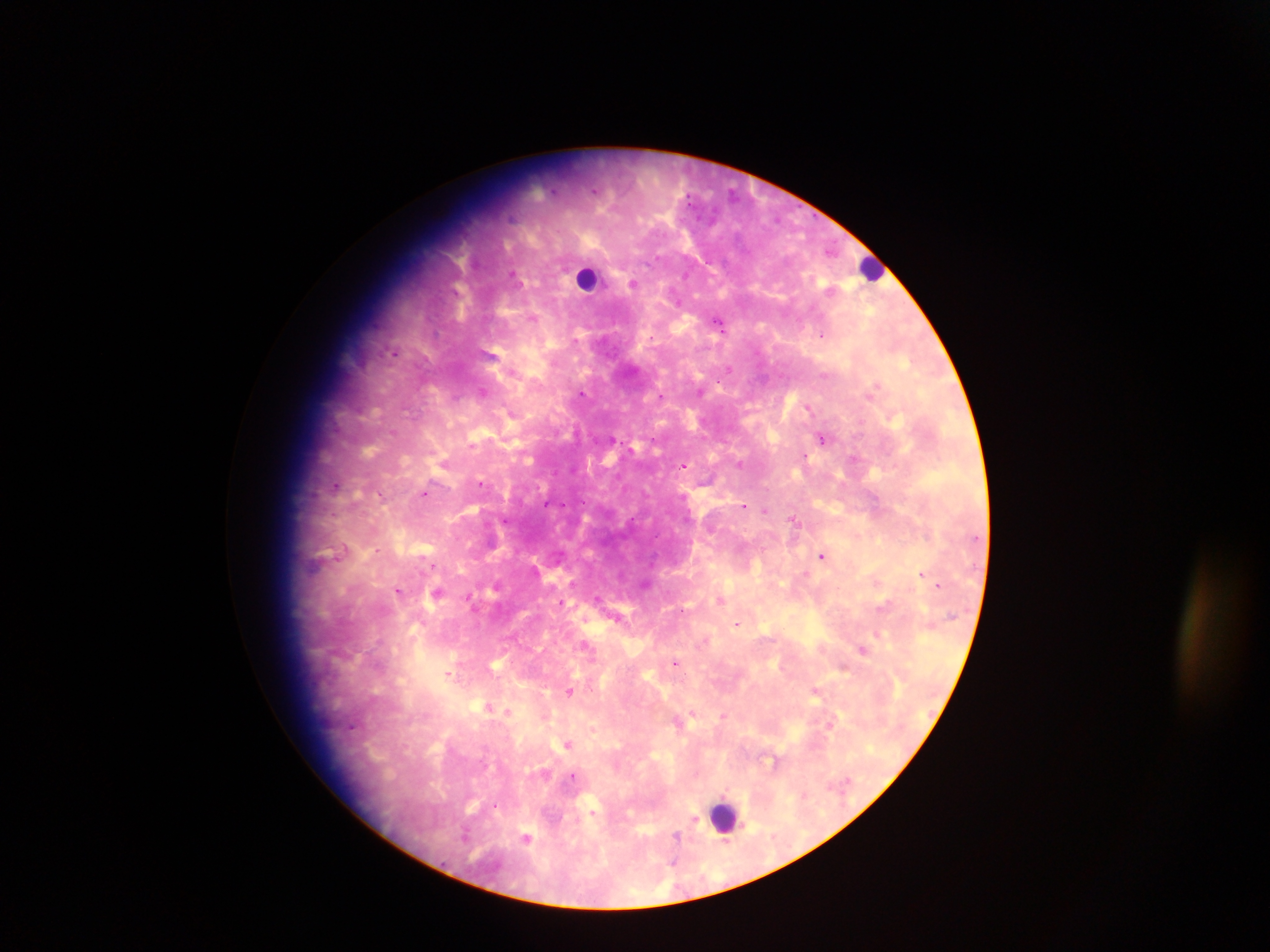
malaria_parasite_locations: 'approximate centers as x y in pixels: 633 283; 533 318; 720 321; 823 334; 394 352; 484 391; 582 393; 661 396; 808 407; 512 414; 822 437; 854 459; 445 463; 740 463; 683 465; 481 483; 337 485; 426 493; 744 506; 765 511; 794 520; 505 521; 377 550; 823 556; 431 565; 923 574; 647 583; 498 585; 938 585; 399 590; 437 592; 470 599; 721 599; 561 602; 617 618; 737 623; 879 634; 705 640; 586 646; 863 649; 676 662; 449 672; 570 691; 815 692; 489 707; 508 711; 693 713; 723 716; 830 724; 353 725; 568 744; 773 760; 574 777; 592 812; 694 820; 527 836; 678 837'
country: Ghana
image_size: 1270×952 pixels
capture: mobile-phone photograph through a microscope
field_of_view: single
leukocyte_locations: 'approximate centers as x y in pixels: 870 268; 587 277; 723 816'
preparation: thick blood film